Locate every malaria parasite and every leukocyte.
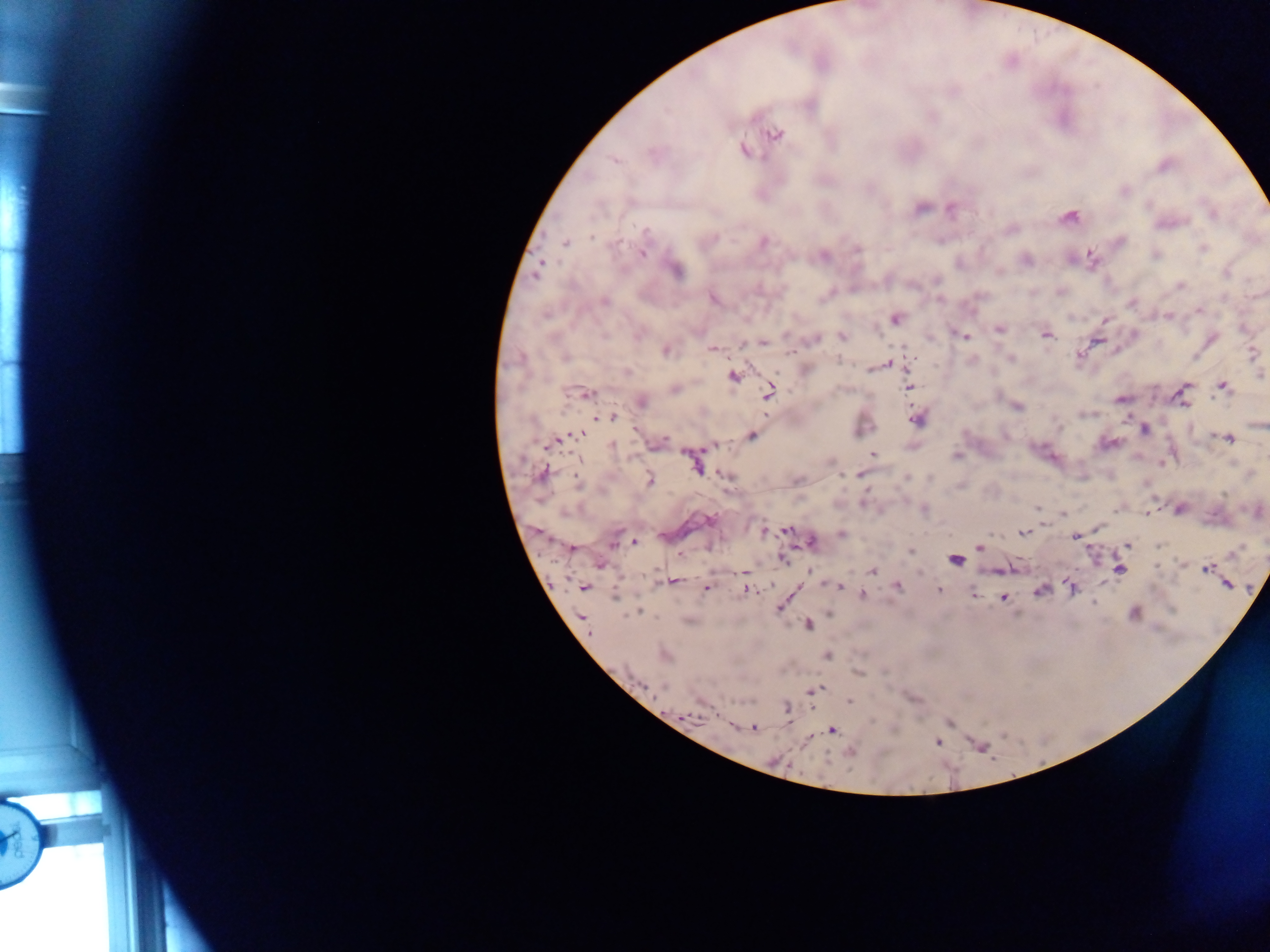

Approximate centers as {x, y} in pixels.
Malaria parasites: {775, 134}, {744, 151}, {614, 160}, {1163, 166}, {921, 209}, {951, 209}, {1070, 217}, {646, 232}, {713, 239}, {566, 242}, {764, 242}, {858, 248}, {1203, 248}, {642, 254}, {1155, 255}, {823, 256}, {1091, 257}, {1026, 259}, {540, 265}, {536, 270}, {677, 271}, {999, 272}, {1226, 273}, {937, 280}, {1180, 286}, {713, 299}, {604, 302}, {1131, 302}, {1199, 310}, {1168, 316}, {895, 319}, {1106, 320}, {999, 330}, {1046, 334}, {787, 335}, {965, 335}, {842, 337}, {814, 338}, {763, 342}, {743, 343}, {712, 349}, {667, 351}, {1251, 353}, {1079, 355}, {565, 357}, {1011, 359}, {839, 361}, {885, 364}, {626, 372}, {1261, 375}, {734, 377}, {1223, 386}, {908, 387}, {675, 388}, {769, 392}, {587, 395}, {1121, 399}, {642, 402}, {1018, 407}, {613, 417}, {600, 418}, {916, 420}, {1144, 430}, {576, 435}, {751, 435}, {1227, 438}, {658, 442}, {549, 444}, {612, 445}, {714, 445}, {873, 453}, {955, 456}, {694, 463}, {543, 473}, {860, 474}, {726, 476}, {907, 478}, {649, 481}, {796, 481}, {577, 483}, {863, 503}, {1037, 508}, {923, 509}, {1178, 509}, {1148, 511}, {1062, 515}, {765, 531}, {787, 531}, {1023, 533}, {841, 534}, {1075, 537}, {614, 541}, {635, 542}, {813, 542}, {1126, 545}, {980, 547}, {572, 549}, {911, 552}, {1233, 553}, {680, 554}, {782, 559}, {955, 560}, {1206, 568}, {1119, 570}, {872, 571}, {745, 573}, {674, 581}, {1228, 584}, {897, 586}, {584, 587}, {837, 587}, {1072, 587}, {706, 588}, {747, 590}, {939, 591}, {1040, 591}, {862, 594}, {614, 597}, {1005, 598}, {1093, 603}, {780, 608}, {638, 612}, {1134, 612}, {582, 617}, {688, 620}, {808, 625}, {665, 654}, {827, 656}, {661, 686}, {814, 690}, {849, 701}, {787, 710}, {689, 717}, {753, 728}, {832, 730}, {850, 752}, {773, 761}.
No leukocytes observed.

country = Ghana
capture = mobile-phone photograph through a microscope
image size = 1270×952 pixels
field of view = single
preparation = thick blood film